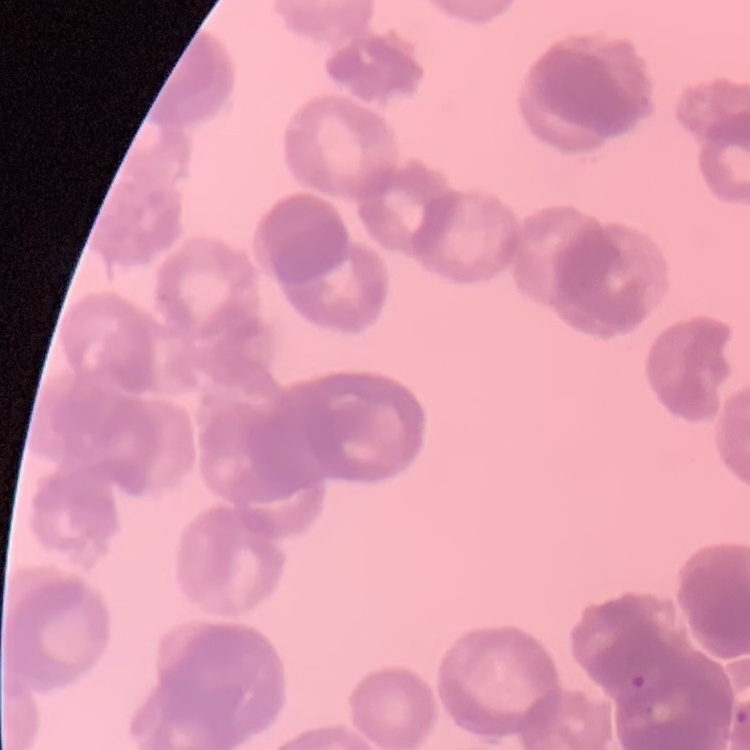

erythrocyte morphology = rouleaux formation
stain = Field's or Giemsa
image type = one tile cut from a larger photomicrograph
preparation = thin blood smear